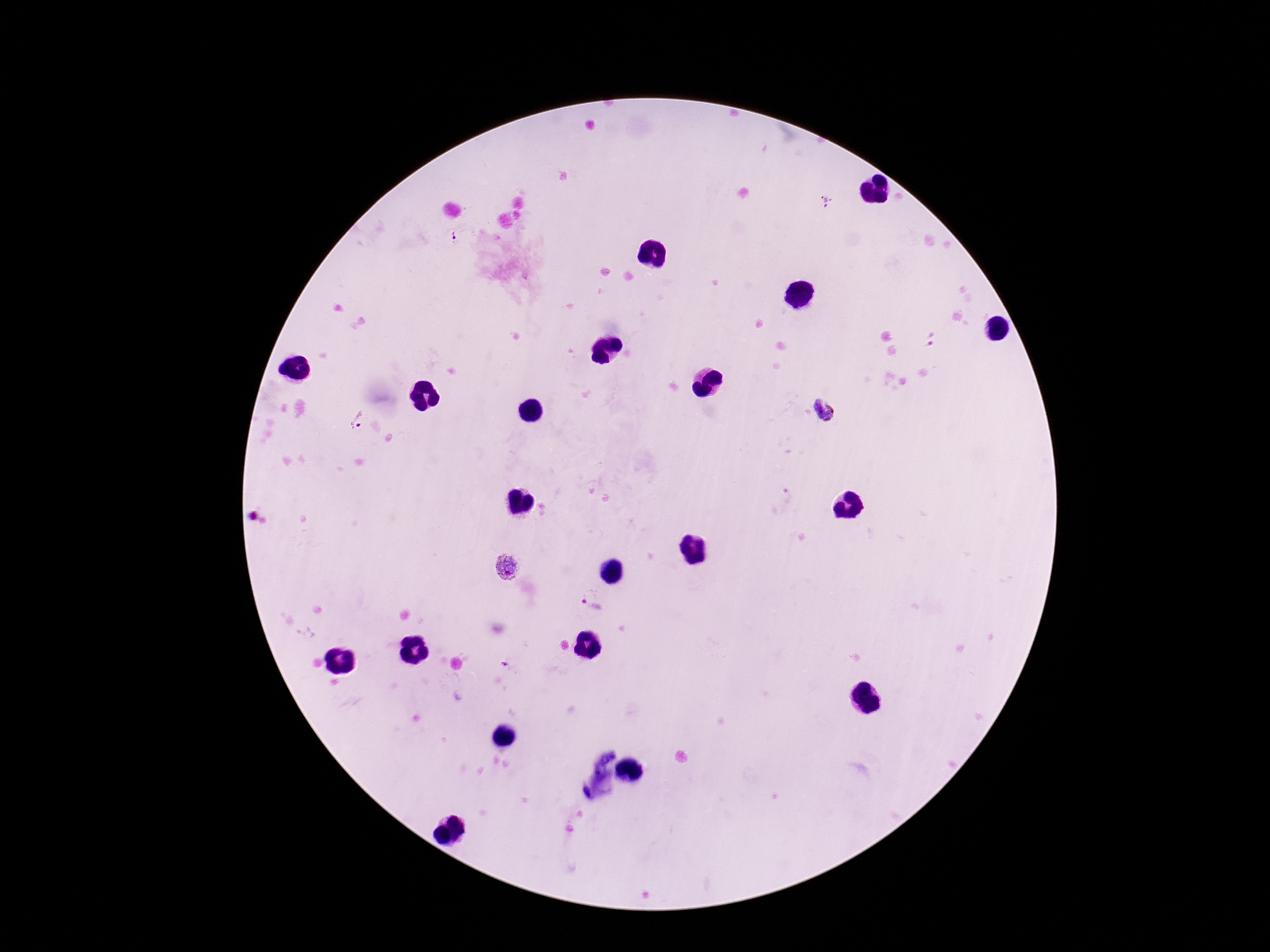

Approximate centers as (x, y) in pixels. Plasmodium parasite locations: (825, 201), (453, 237), (824, 412), (357, 422), (509, 570), (594, 604). Giemsa-stained preparation. Single field of view. Photographed through the microscope eyepiece with a smartphone camera. Patient malaria status: positive. Thick peripheral-blood smear. Image is 1270×952 pixels. 100x magnification.